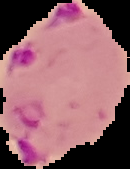
From a thin blood smear. Malaria status: parasitized. Image is 130×169 pixels. Cell region segmented out of the field of view; the surrounding area is masked to black.